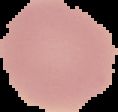

Summary:
  - Image type: cell region segmented out of the field of view; surrounding area masked to black
  - Preparation: thin blood smear
  - Image size: 118×112 pixels
  - Malaria status: uninfected